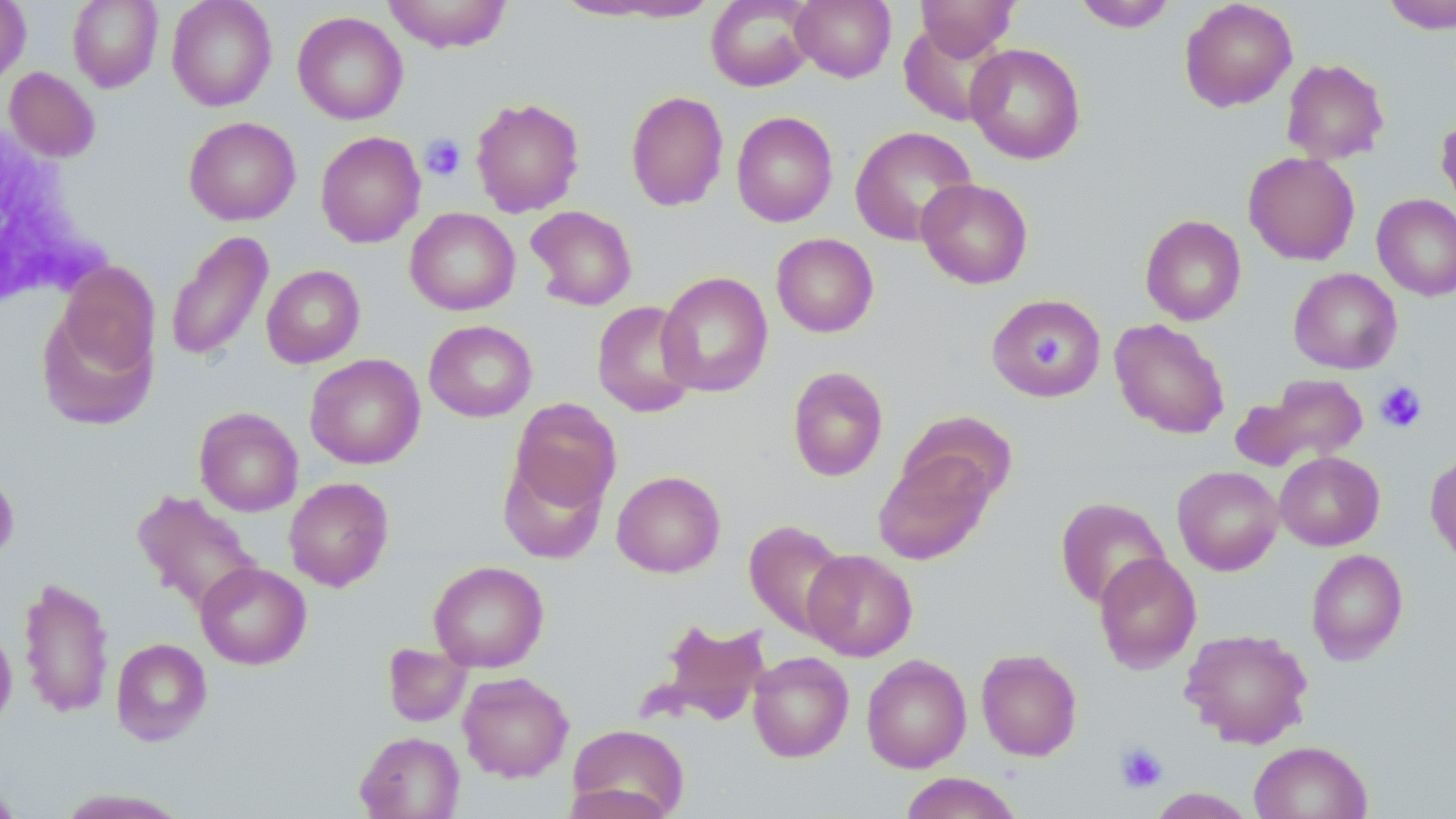
Summary:
  - Coordinate format: approximate bounding boxes as named x1/y1/x2/y2 corners in pixels
  - White blood cell locations: (x1=1, y1=117, x2=101, y2=309)
  - Uninfected red blood cell locations: (x1=68, y1=0, x2=163, y2=92), (x1=166, y1=0, x2=277, y2=111), (x1=382, y1=0, x2=512, y2=53), (x1=544, y1=0, x2=704, y2=22), (x1=706, y1=0, x2=816, y2=92), (x1=791, y1=0, x2=896, y2=83), (x1=915, y1=0, x2=1019, y2=59), (x1=1074, y1=0, x2=1177, y2=32), (x1=1179, y1=0, x2=1298, y2=112), (x1=1381, y1=0, x2=1456, y2=33), (x1=0, y1=1, x2=31, y2=89), (x1=292, y1=12, x2=408, y2=125), (x1=898, y1=22, x2=1008, y2=127), (x1=965, y1=42, x2=1086, y2=164), (x1=1281, y1=59, x2=1390, y2=164), (x1=4, y1=67, x2=100, y2=162), (x1=625, y1=90, x2=728, y2=211), (x1=470, y1=97, x2=584, y2=217), (x1=731, y1=111, x2=837, y2=227), (x1=1435, y1=112, x2=1456, y2=214), (x1=184, y1=116, x2=301, y2=225), (x1=849, y1=126, x2=977, y2=245), (x1=315, y1=131, x2=426, y2=248), (x1=1243, y1=152, x2=1360, y2=265), (x1=916, y1=178, x2=1033, y2=289), (x1=1372, y1=194, x2=1456, y2=301), (x1=526, y1=206, x2=637, y2=311), (x1=405, y1=207, x2=520, y2=315), (x1=1140, y1=214, x2=1246, y2=325), (x1=165, y1=230, x2=273, y2=363), (x1=771, y1=233, x2=878, y2=337), (x1=53, y1=262, x2=161, y2=380), (x1=261, y1=264, x2=365, y2=368), (x1=1288, y1=268, x2=1402, y2=374), (x1=657, y1=271, x2=772, y2=397), (x1=986, y1=292, x2=1106, y2=402), (x1=592, y1=300, x2=699, y2=418), (x1=36, y1=302, x2=159, y2=431), (x1=1109, y1=318, x2=1230, y2=439), (x1=424, y1=320, x2=537, y2=422), (x1=305, y1=353, x2=425, y2=469), (x1=787, y1=366, x2=888, y2=482), (x1=1232, y1=373, x2=1369, y2=473), (x1=508, y1=399, x2=621, y2=514), (x1=194, y1=407, x2=304, y2=516), (x1=898, y1=410, x2=1019, y2=508), (x1=873, y1=450, x2=996, y2=565), (x1=1274, y1=451, x2=1384, y2=550), (x1=1425, y1=451, x2=1456, y2=568), (x1=498, y1=452, x2=609, y2=564), (x1=1172, y1=466, x2=1283, y2=575), (x1=0, y1=467, x2=20, y2=565), (x1=611, y1=470, x2=726, y2=577), (x1=284, y1=477, x2=394, y2=592), (x1=131, y1=489, x2=263, y2=615), (x1=1055, y1=496, x2=1170, y2=609), (x1=744, y1=519, x2=851, y2=639), (x1=802, y1=549, x2=918, y2=661), (x1=1306, y1=549, x2=1409, y2=665), (x1=1093, y1=551, x2=1202, y2=673), (x1=428, y1=560, x2=549, y2=672), (x1=195, y1=562, x2=311, y2=670), (x1=18, y1=576, x2=114, y2=719), (x1=654, y1=618, x2=771, y2=725), (x1=0, y1=622, x2=17, y2=733), (x1=1179, y1=628, x2=1314, y2=749), (x1=111, y1=638, x2=212, y2=746), (x1=382, y1=643, x2=471, y2=727), (x1=976, y1=648, x2=1083, y2=761), (x1=748, y1=652, x2=854, y2=762), (x1=861, y1=654, x2=972, y2=773), (x1=458, y1=672, x2=574, y2=782), (x1=567, y1=724, x2=690, y2=816), (x1=354, y1=731, x2=465, y2=819), (x1=1249, y1=741, x2=1372, y2=818), (x1=899, y1=772, x2=1024, y2=819), (x1=0, y1=778, x2=23, y2=818), (x1=560, y1=783, x2=678, y2=819), (x1=54, y1=788, x2=192, y2=818), (x1=1146, y1=788, x2=1257, y2=818)
  - Platelet locations: (x1=420, y1=133, x2=466, y2=180), (x1=1030, y1=334, x2=1068, y2=369), (x1=1375, y1=381, x2=1427, y2=433), (x1=1115, y1=742, x2=1168, y2=793)
  - Slide-level diagnosis: no evidence of blood parasites
  - Preparation: thin blood film
  - Magnification: 1000x
  - Field of view: single
  - Image size: 1456×819 pixels
  - Modality: optical microscopy
  - Stain: May-Grünwald-Giemsa